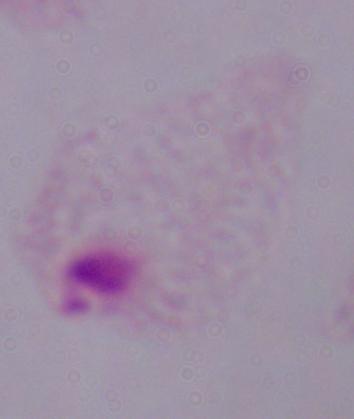

modality: photomicrograph
identification: trichomonad
magnification: 1000x